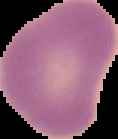

From a thin blood film. Image is 118×139 pixels. Segmented cell region on a black background. Malaria status: uninfected.